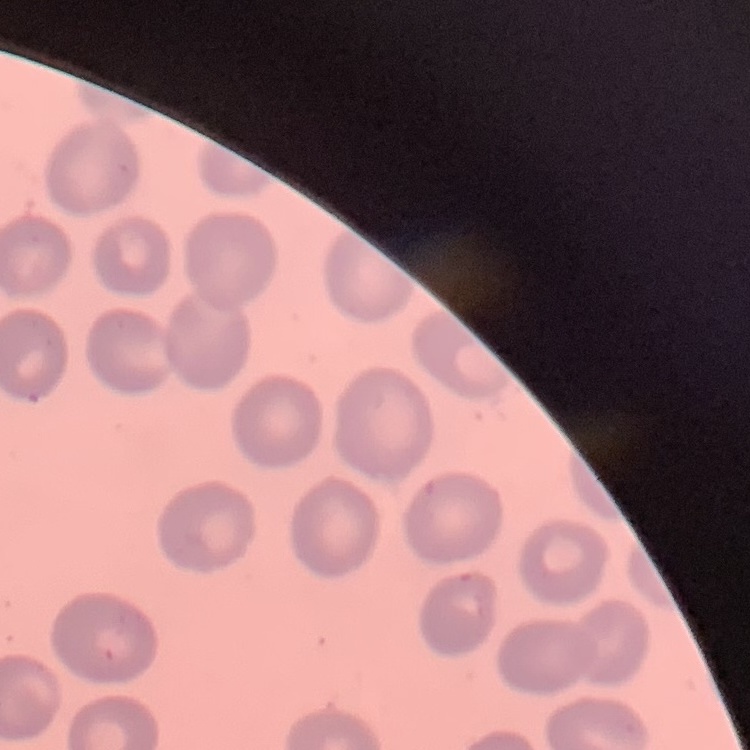
Summary:
  - Erythrocyte morphology: no rouleaux formation
  - Stain: Field's or Giemsa
  - Image type: one tile cut from a larger photomicrograph
  - Preparation: thin blood smear